Report the malaria status.
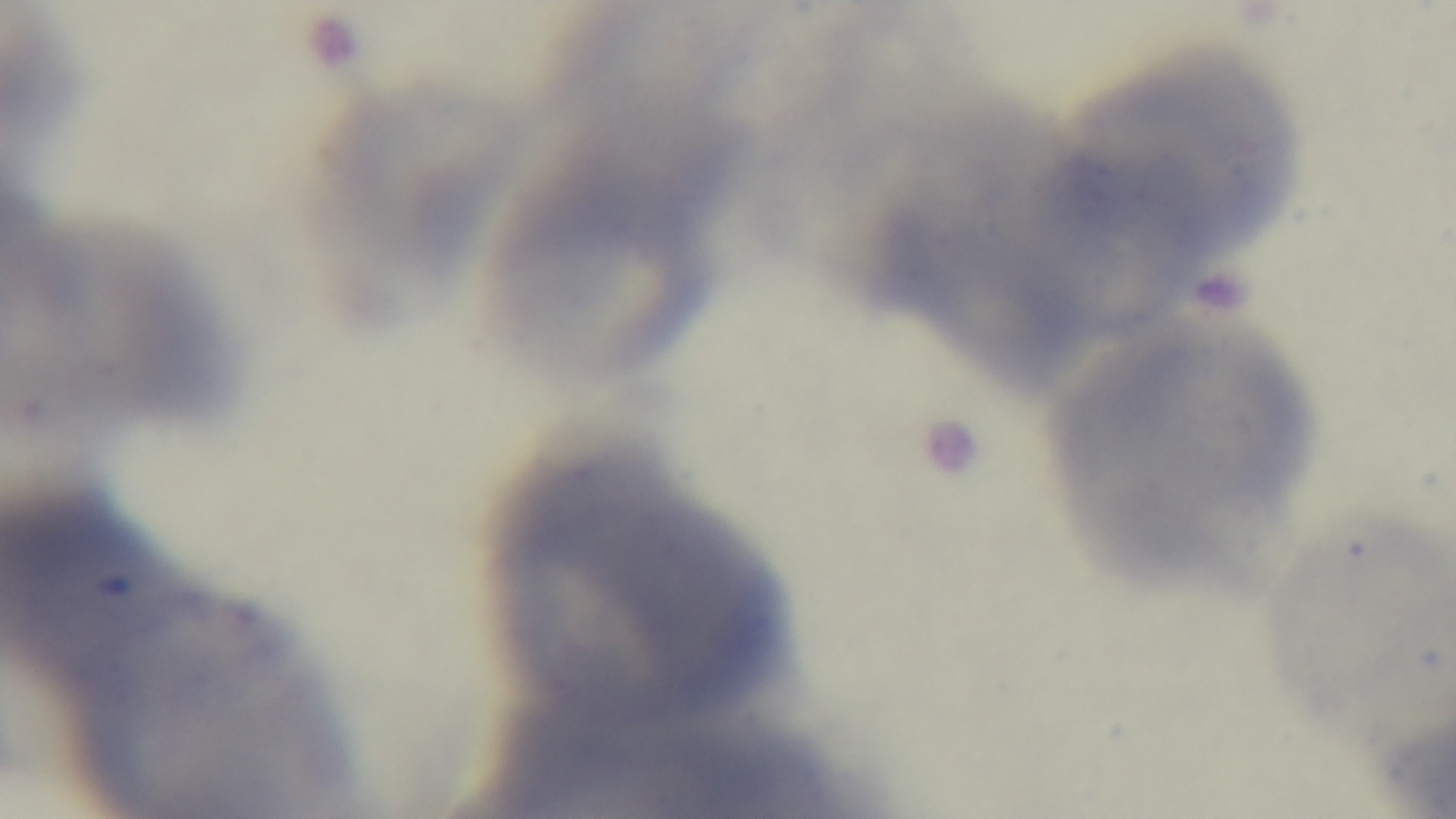

It is uninfected.

Summary:
  - Modality: light microscopy
  - Stain: Giemsa
  - Objective: 100x oil immersion
  - Capture: mounted 4K digital camera
  - Field of view: one from the slide
  - Preparation: thin blood film